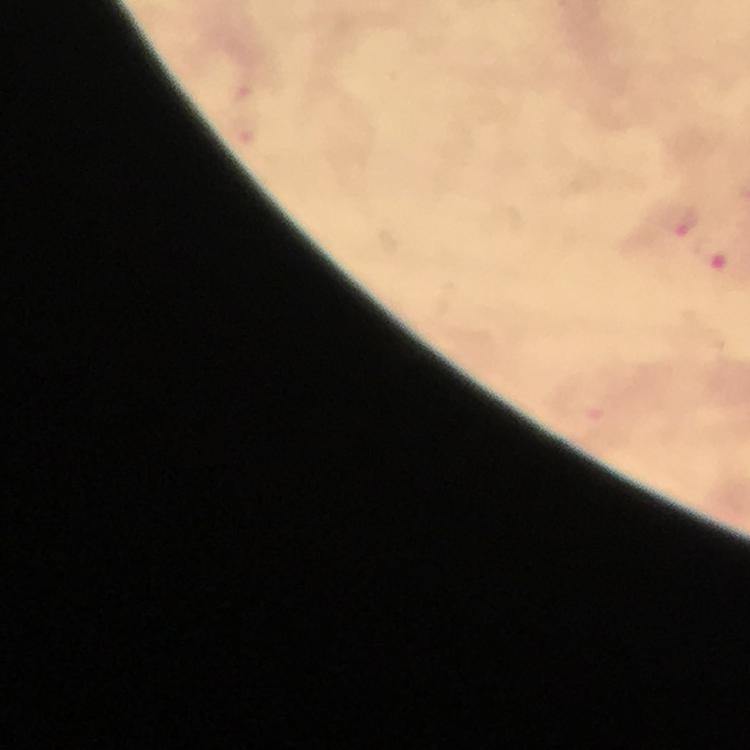
Approximate centers as {x, y} in pixels. Malaria parasite locations: {681, 224}. Cropped region of a single field of view. Immersion oil applied. At 100x magnification. Thick blood film. Giemsa stain. Image is 750×750 pixels. From a diagnostic examination for malaria. Smartphone photograph taken through a microscope.